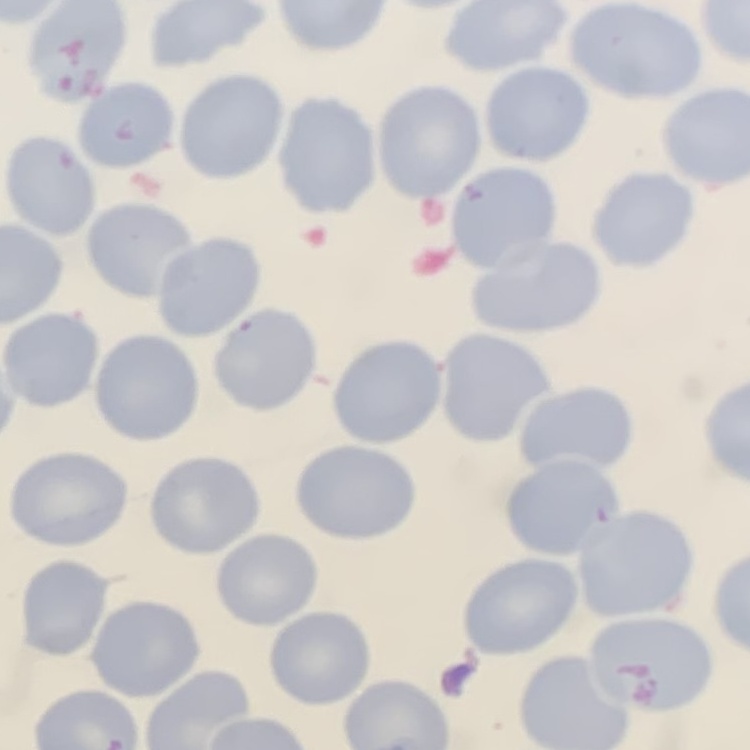
The red blood cells show no rouleaux formation. Thin blood smear. One tile cut from a larger photomicrograph. Stained with either Field's or Giemsa.